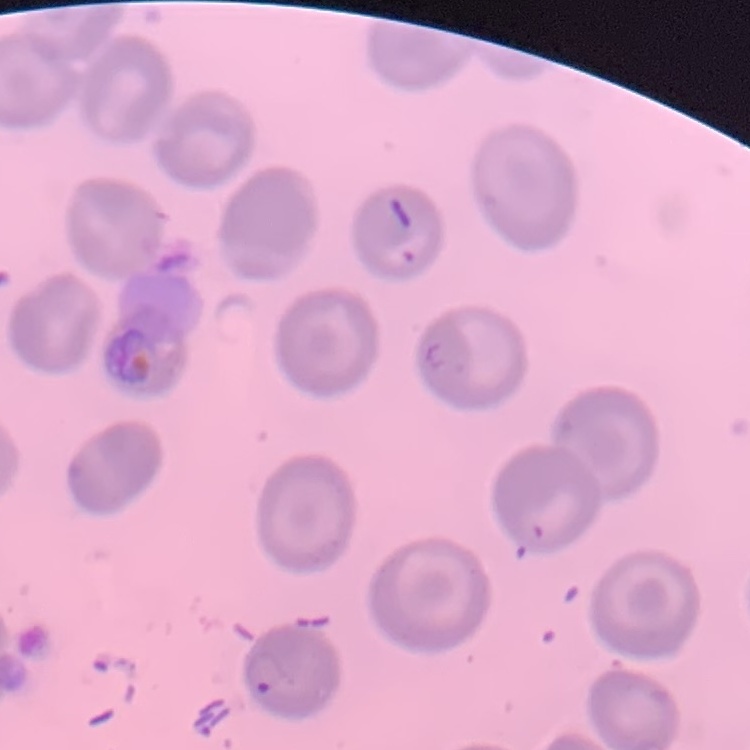
{
  "erythrocyte_morphology": "no rouleaux formation",
  "stain": "Field's or Giemsa",
  "preparation": "thin blood film",
  "image_type": "one tile cut from a larger photomicrograph"
}